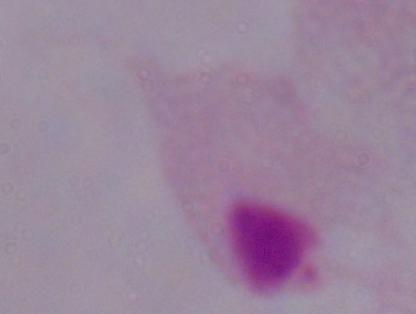

identification: trichomonad
magnification: 1000x
modality: photomicrograph